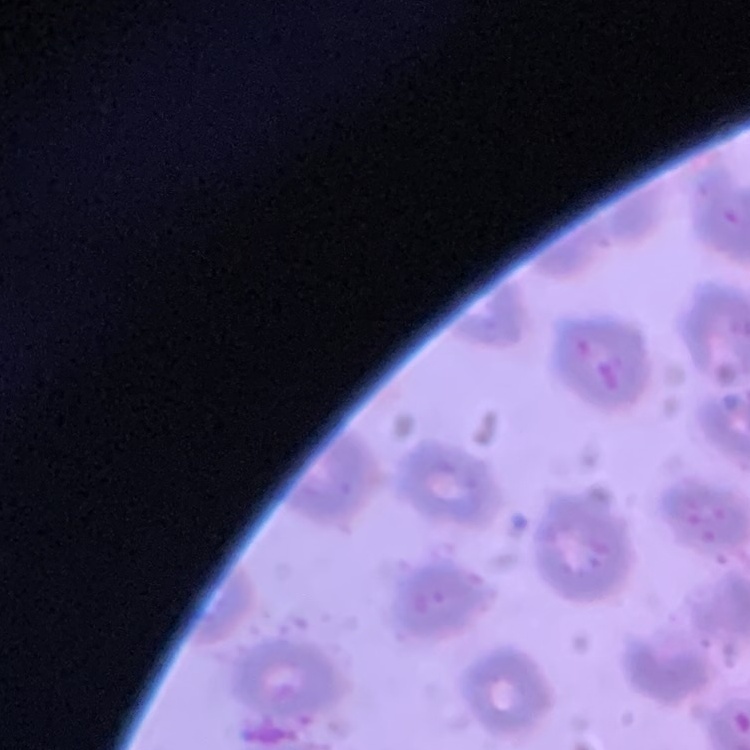

The erythrocytes exhibit no rouleaux formation. Field's or Giemsa stain. Thin blood film. One tile cut from a larger photomicrograph.